Name the blood parasite species.
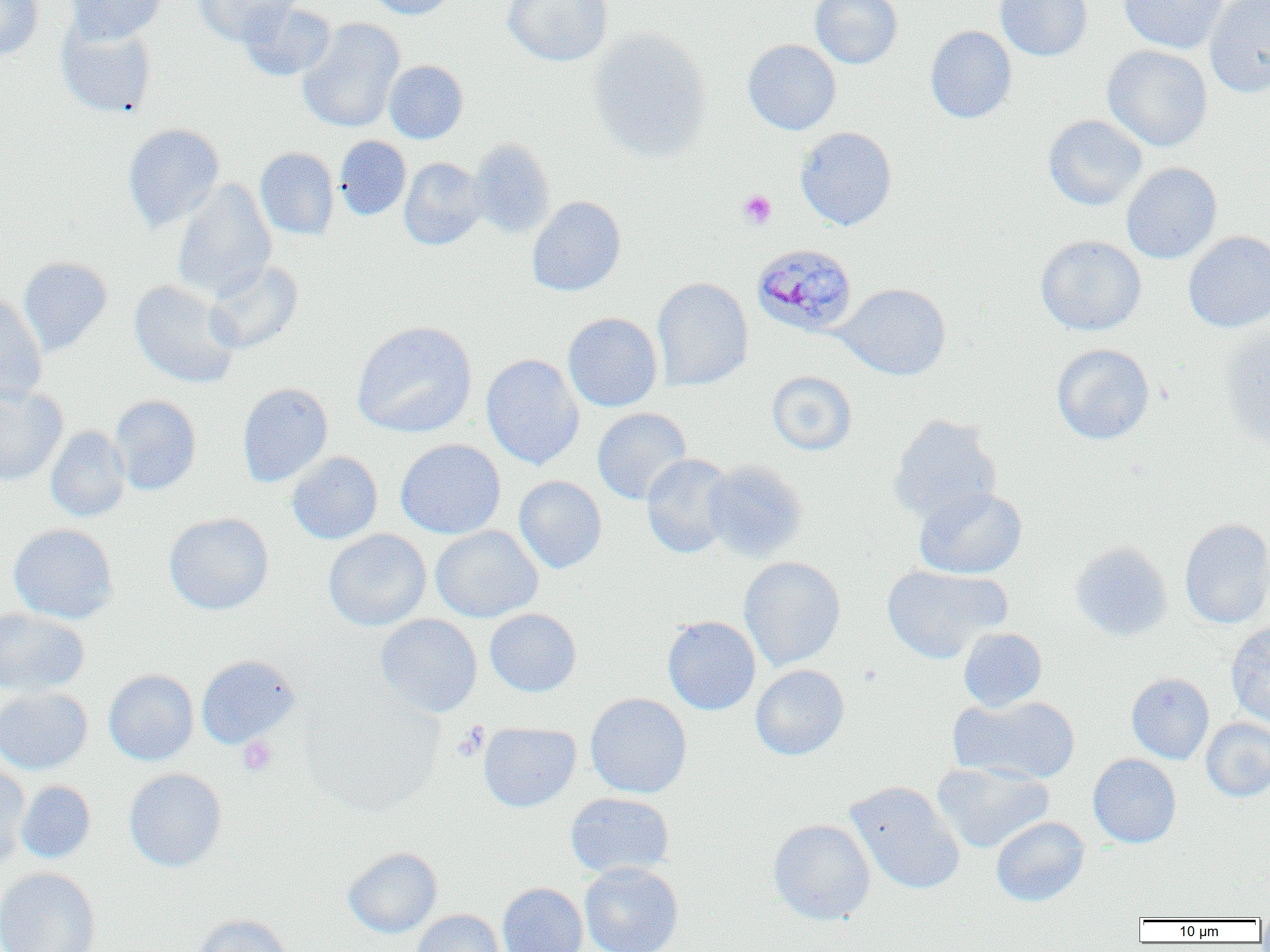
Plasmodium malariae.

{
  "modality": "optical microscopy",
  "platelet_locations": "approximate bounding boxes as (x1, y1, x2, y2) in pixels: (737, 190, 777, 229), (452, 723, 489, 762), (238, 736, 277, 776)",
  "preparation": "thin blood film",
  "magnification": "1000x",
  "uninfected_red_blood_cell_locations": "approximate bounding boxes as (x1, y1, x2, y2) in pixels: (0, 0, 43, 61), (67, 0, 167, 43), (192, 0, 300, 45), (365, 0, 458, 20), (503, 0, 612, 66), (810, 0, 903, 69), (995, 0, 1092, 61), (1119, 0, 1227, 53), (1205, 0, 1270, 97), (239, 1, 336, 81), (298, 18, 404, 133), (56, 19, 157, 118), (925, 26, 1017, 123), (588, 28, 712, 161), (743, 39, 841, 135), (1102, 45, 1213, 151), (384, 60, 468, 143), (1043, 115, 1147, 211), (123, 123, 224, 232), (795, 126, 897, 231), (334, 136, 411, 220), (468, 139, 555, 238), (255, 147, 339, 240), (399, 158, 486, 250), (1121, 162, 1222, 264), (172, 179, 276, 301), (527, 196, 626, 296), (1184, 231, 1270, 332), (1035, 235, 1146, 335), (18, 257, 112, 356), (204, 260, 303, 354), (651, 277, 753, 391), (130, 280, 240, 388), (835, 283, 951, 380), (0, 291, 47, 403), (563, 312, 662, 412), (352, 321, 477, 438), (1219, 326, 1270, 450), (1051, 343, 1154, 445), (481, 353, 584, 470), (766, 371, 857, 455), (237, 382, 332, 487), (0, 384, 68, 486), (110, 395, 201, 495), (592, 407, 691, 505), (887, 414, 1001, 524), (45, 426, 130, 522), (395, 439, 506, 539), (287, 451, 382, 544), (641, 453, 737, 558), (703, 460, 808, 562), (513, 476, 606, 573), (914, 486, 1027, 579), (163, 512, 274, 615), (1179, 518, 1270, 629), (8, 523, 118, 624), (431, 525, 543, 623), (323, 529, 431, 631), (1069, 541, 1172, 641), (739, 556, 845, 671), (881, 564, 1010, 663), (0, 607, 90, 697), (484, 608, 582, 696), (375, 614, 482, 717), (662, 615, 761, 715), (1226, 622, 1270, 727), (958, 627, 1047, 711), (196, 655, 301, 748), (750, 664, 850, 760), (103, 669, 198, 765), (1126, 673, 1214, 764), (0, 687, 92, 774), (302, 690, 444, 816), (584, 693, 692, 798), (949, 695, 1080, 785), (1201, 718, 1270, 802), (478, 722, 580, 812), (1088, 754, 1182, 848), (931, 761, 1054, 853), (0, 763, 30, 868), (124, 768, 226, 871), (16, 781, 96, 863), (845, 781, 965, 895), (565, 792, 674, 878), (990, 816, 1090, 907), (768, 819, 875, 924), (343, 847, 443, 938), (579, 861, 684, 952), (0, 867, 101, 952), (497, 882, 588, 952), (410, 909, 506, 952), (192, 913, 293, 952)",
  "image_size": "1270×952 pixels",
  "field_of_view": "one of a larger specimen",
  "plasmodium_malariae_infected_red_blood_cell_locations": "approximate bounding boxes as (x1, y1, x2, y2) in pixels: (751, 244, 858, 337)"
}